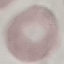

Summary:
  - Malaria status: uninfected
  - Capture: smartphone through the microscope eyepiece
  - Stain: Giemsa
  - Preparation: thin blood film
  - Image type: cell patch, automatically extracted from a larger field of view and resized to 64 × 64 pixels